Assess this cell for malaria.
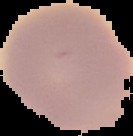
It is uninfected.

Cell region segmented out of the field of view; the surrounding area is masked to black. From a thin blood film. Image is 133×136 pixels.